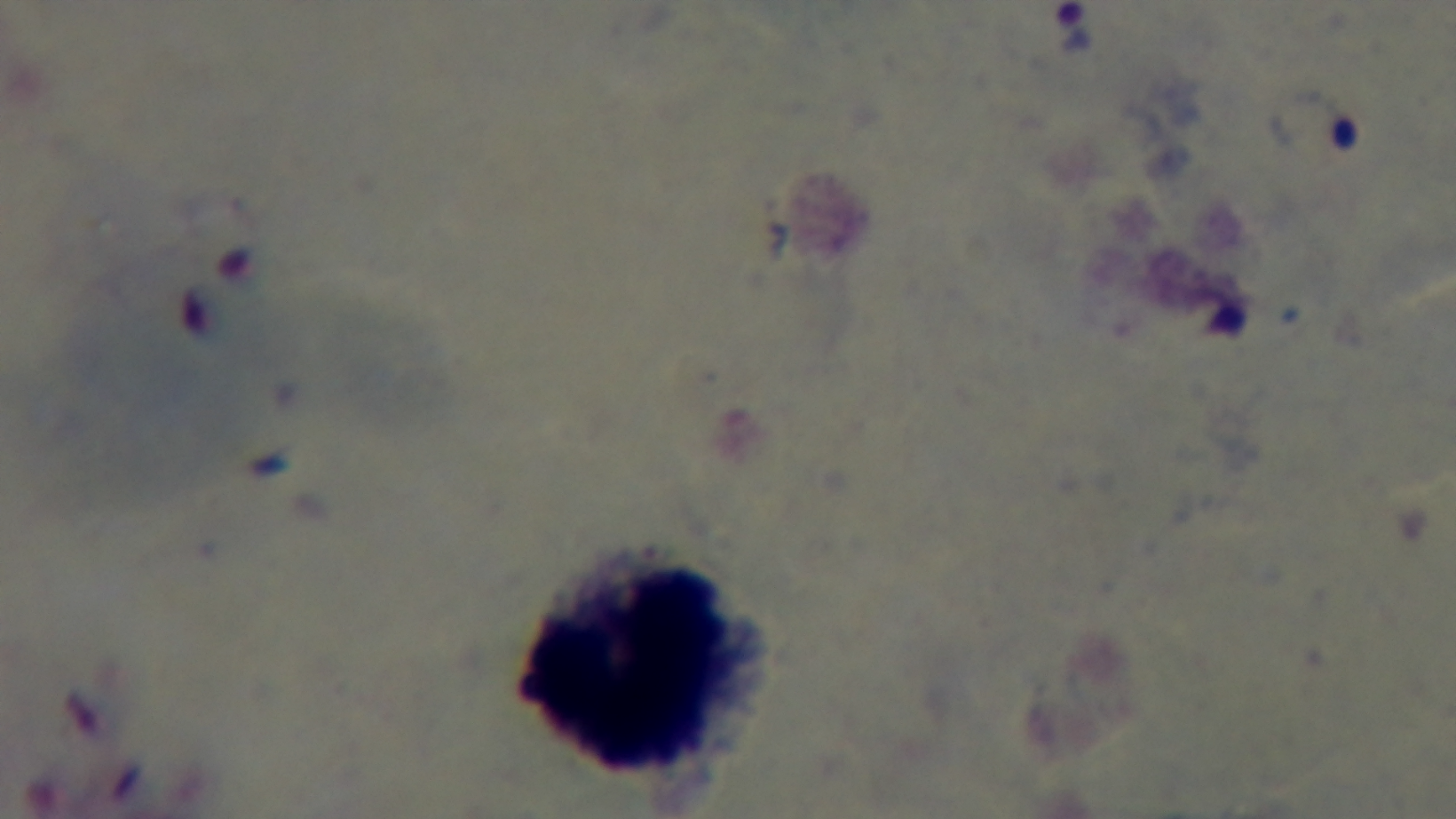
Preparation: thick blood film. One field from the slide. Giemsa stain. Captured with a mounted 4K digital camera. Light microscopy. 100x oil-immersion objective. Malaria status: infected.